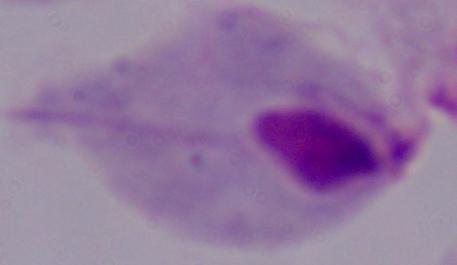
Summary:
  - Modality: photomicrograph
  - Identification: trichomonad
  - Magnification: 1000x